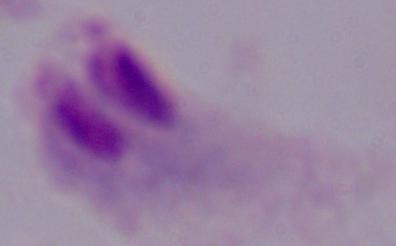
Micrograph. A trichomonad is seen. Captured at 1000x magnification.